Report the malaria status of this cell.
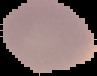
Uninfected.

image type = segmented cell region with the area outside set to black
image size = 97×76 pixels
preparation = thin blood smear